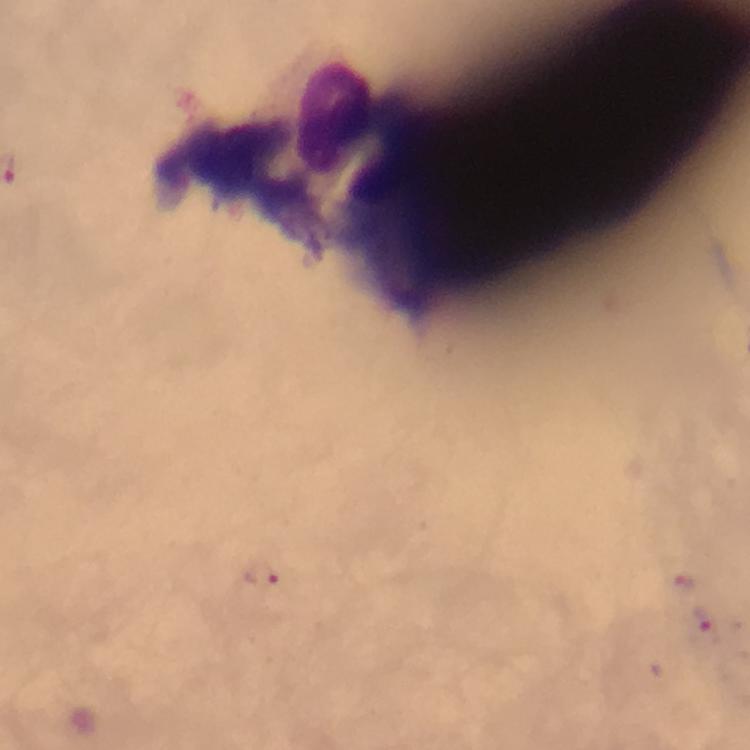

Approximate centers as (x, y) in pixels. Leukocyte locations: (323, 111). Plasmodium parasite locations: (261, 575), (682, 581), (705, 623). Giemsa stain. Immersion oil applied. At 100x magnification. Image is 750×750 pixels. From a malaria diagnostic workup. Photographed with a smartphone mounted on the microscope. A crop from one field of view. Thick smear.